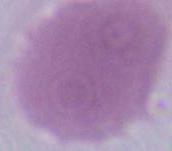
Captured at 1000x magnification. An erythrocyte is seen. Micrograph.